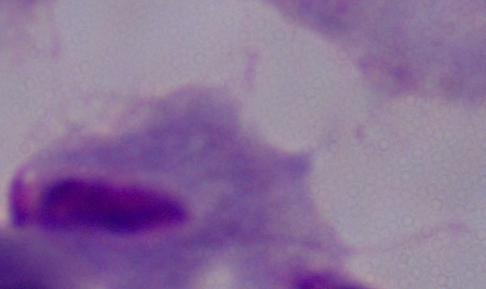 1000x magnification. A trichomonad is shown. Photomicrograph.